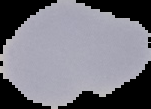 Segmented cell region on a black background. From a thin blood film. Image is 151×109 pixels. Result: no Plasmodium parasites detected.